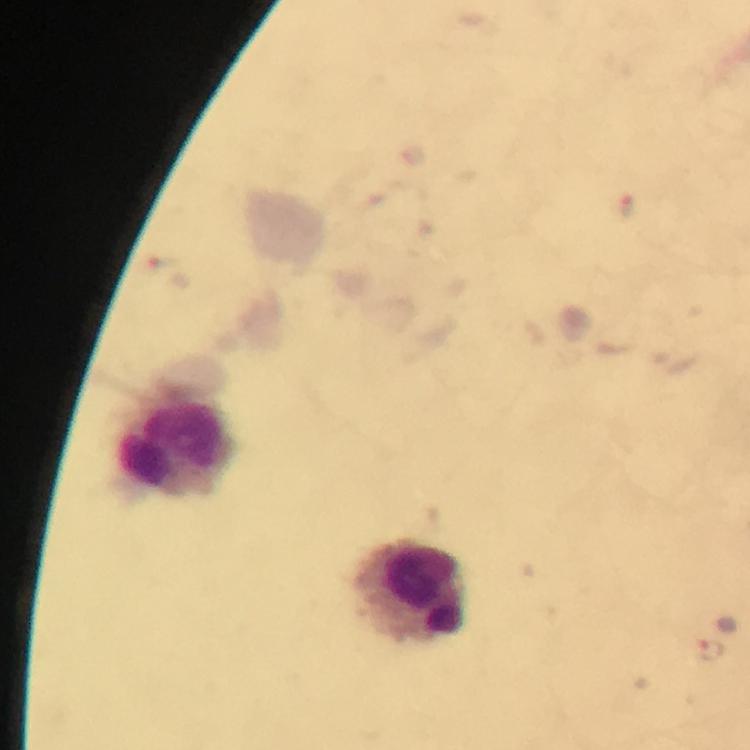
immersion_oil: applied
cropped_from: a single field of view
leukocyte_locations: 'approximate centers as (x, y) in pixels: (179, 450), (414, 593)'
preparation: thick blood film
malaria_parasite_locations: 'approximate centers as (x, y) in pixels: (628, 205), (708, 650)'
image_size: 750×750 pixels
context: from a malaria diagnostic workup
magnification: 100x
capture: smartphone photograph through a microscope
stain: Giemsa